Classify this cell by malaria status.
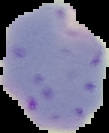

It is parasitized.

Image is 109×133 pixels. From a thin blood smear. The area outside the segmented cell region is set to black.